Report the malaria status of this cell.
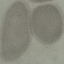

It is uninfected.

stain = Giemsa
preparation = thin blood smear
image type = automatically extracted cell patch, resized to 64 × 64 pixels
capture = smartphone through the microscope eyepiece